Classify this cell by malaria status.
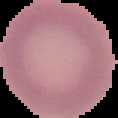

Uninfected.

Summary:
  - Image type: segmented cell region on a black background
  - Preparation: thin blood smear
  - Image size: 118×118 pixels